Classify this cell by malaria status.
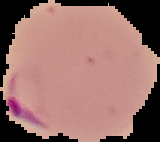
It is parasitized.

Summary:
  - Image type: segmented cell region on a black background
  - Preparation: thin blood smear
  - Image size: 160×142 pixels